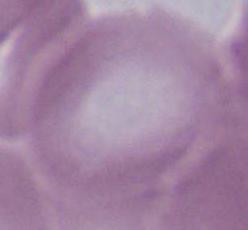

modality = micrograph
magnification = 1000x
identification = erythrocyte